Outline each blood parasite and name the species.
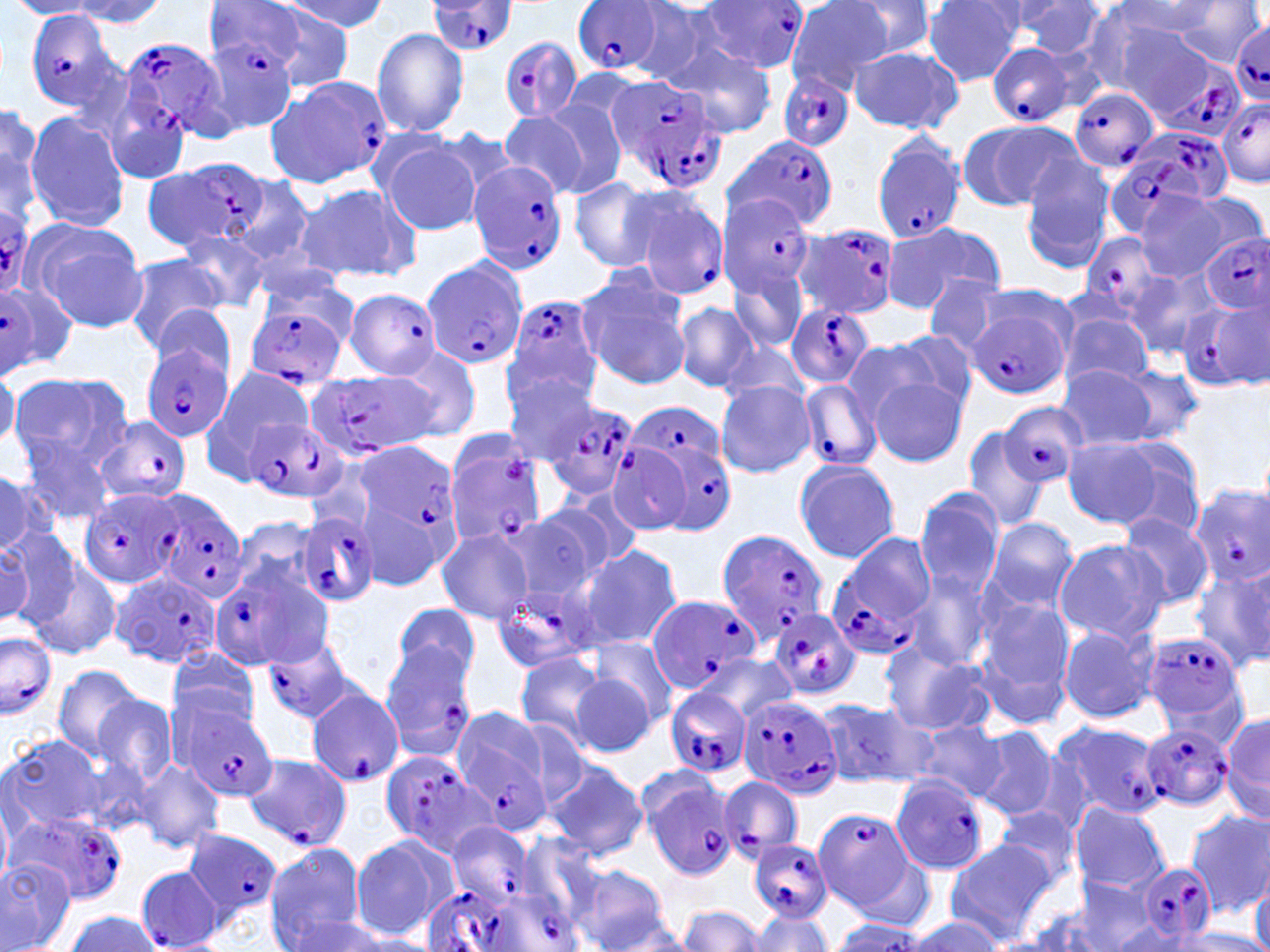

Approximate bounding boxes as (x1,y1)-(x2,y2) corner pairs in pixels.
Plasmodium falciparum-infected red blood cells: (427,0)-(517,55), (699,1)-(808,77), (571,3)-(668,75), (23,10)-(124,112), (1231,22)-(1270,105), (201,33)-(298,130), (120,36)-(234,140), (500,37)-(582,123), (985,41)-(1073,128), (1161,63)-(1245,138), (776,72)-(856,152), (269,77)-(392,188), (604,77)-(726,196), (101,86)-(192,187), (1069,87)-(1161,174), (1218,100)-(1270,187), (1128,127)-(1234,209), (728,134)-(840,234), (871,137)-(968,246), (144,155)-(270,251), (467,159)-(568,273), (645,186)-(728,299), (720,193)-(817,296), (0,194)-(36,295), (798,220)-(904,319), (1201,232)-(1270,312), (1085,233)-(1180,335), (422,258)-(528,369), (2,283)-(61,374), (342,287)-(444,375), (506,295)-(602,400), (1184,302)-(1270,392), (245,303)-(346,392), (787,305)-(874,391), (966,308)-(1068,400), (141,342)-(233,442), (306,373)-(432,461), (798,377)-(881,471), (532,395)-(640,499), (625,396)-(728,484), (1001,403)-(1088,488), (244,416)-(347,504), (94,417)-(192,505), (642,433)-(735,537), (444,436)-(546,548), (607,443)-(691,533), (353,444)-(463,550), (1190,486)-(1270,584), (79,488)-(182,589), (153,495)-(250,601), (293,511)-(380,608), (715,529)-(829,641), (824,532)-(936,657), (211,566)-(317,671), (112,570)-(221,669), (490,573)-(603,676), (648,593)-(758,693), (769,608)-(861,699), (0,630)-(57,721), (1143,630)-(1247,735), (259,634)-(349,723), (379,643)-(476,761), (306,684)-(403,790), (665,688)-(752,778), (737,693)-(845,801), (176,703)-(278,803), (453,710)-(551,827), (1052,720)-(1164,822), (1141,722)-(1236,814), (378,751)-(490,858), (241,752)-(353,850), (641,772)-(737,880), (889,776)-(991,875), (720,777)-(804,860), (814,808)-(914,912), (9,809)-(129,908), (447,822)-(536,909), (183,829)-(284,924), (747,838)-(832,922), (1139,861)-(1216,941), (134,864)-(225,952), (418,886)-(546,952), (483,893)-(579,952).
No Plasmodium ovale, Plasmodium malariae, Plasmodium vivax, Babesia divergens, or Trypanosoma brucei observed.

slide-level diagnosis = Plasmodium falciparum
magnification = 1000x
field of view = single
modality = optical microscopy
preparation = thin blood smear
stain = May-Grünwald-Giemsa
image size = 1270×952 pixels
uninfected red blood cell locations = approximate bounding boxes as (x1,y1)-(x2,y2) corner pairs in pixels: (59,0)-(166,28), (277,0)-(385,35), (626,1)-(730,85), (785,1)-(896,93), (924,1)-(1025,85), (1010,1)-(1109,56), (1172,1)-(1263,67), (10,2)-(103,19), (837,2)-(941,61), (1114,2)-(1224,38), (246,3)-(357,90), (1079,5)-(1186,98), (1111,20)-(1198,104), (372,28)-(470,139), (665,42)-(777,135), (848,46)-(962,133), (535,97)-(631,198), (0,98)-(43,199), (499,110)-(591,199), (23,111)-(129,232), (960,120)-(1079,211), (381,136)-(483,235), (1018,153)-(1117,270), (228,177)-(316,268), (569,177)-(668,271), (293,182)-(421,284), (1135,190)-(1231,281), (1181,192)-(1267,274), (23,219)-(147,334), (887,221)-(1007,309), (177,228)-(274,313), (250,243)-(345,307), (121,253)-(230,353), (728,258)-(811,357), (1123,267)-(1222,359), (575,271)-(690,389), (922,278)-(1015,358), (673,303)-(759,391), (149,305)-(241,383), (1058,312)-(1153,393), (887,330)-(979,415), (724,342)-(811,409), (386,343)-(481,441), (0,355)-(18,453), (501,362)-(601,459), (1055,363)-(1158,452), (1108,363)-(1201,442), (202,365)-(314,479), (10,373)-(131,478), (868,376)-(964,467), (715,380)-(816,479), (961,424)-(1052,532), (1107,437)-(1207,537), (1063,439)-(1162,527), (793,458)-(900,563), (0,473)-(46,555), (913,488)-(1005,599), (540,492)-(642,582), (501,504)-(612,602), (1116,512)-(1214,609), (229,515)-(325,602), (984,518)-(1077,614), (0,526)-(74,629), (436,528)-(536,625), (2,534)-(40,624), (1055,538)-(1171,645), (578,545)-(682,650), (24,559)-(120,661), (1192,565)-(1270,673), (903,571)-(994,672), (974,597)-(1077,724), (389,602)-(481,693), (1057,624)-(1160,723), (879,640)-(994,737), (166,647)-(261,734), (515,652)-(608,743), (569,653)-(667,757), (700,654)-(797,726), (52,664)-(146,766), (89,691)-(180,790), (814,696)-(928,789), (1222,714)-(1270,821), (913,721)-(1008,803), (970,725)-(1057,819), (1,732)-(112,835), (132,757)-(226,853), (544,759)-(646,862), (1070,803)-(1171,893), (993,809)-(1079,890), (1185,811)-(1270,916), (349,834)-(457,940), (946,841)-(1056,939), (263,844)-(369,950), (0,855)-(75,951), (572,866)-(672,950), (1250,873)-(1269,952), (1069,877)-(1165,951), (927,882)-(1045,952), (676,904)-(766,951), (1019,905)-(1125,952), (748,910)-(832,951), (58,911)-(165,951), (278,911)-(402,951), (908,917)-(1002,950), (827,919)-(931,949), (1171,929)-(1270,951)